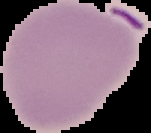
image type = segmented cell region on a black background
preparation = thin blood smear
image size = 151×133 pixels
result = no malaria parasites detected